Give the extent of all Plasmodium falciparum-infected red blood cells.
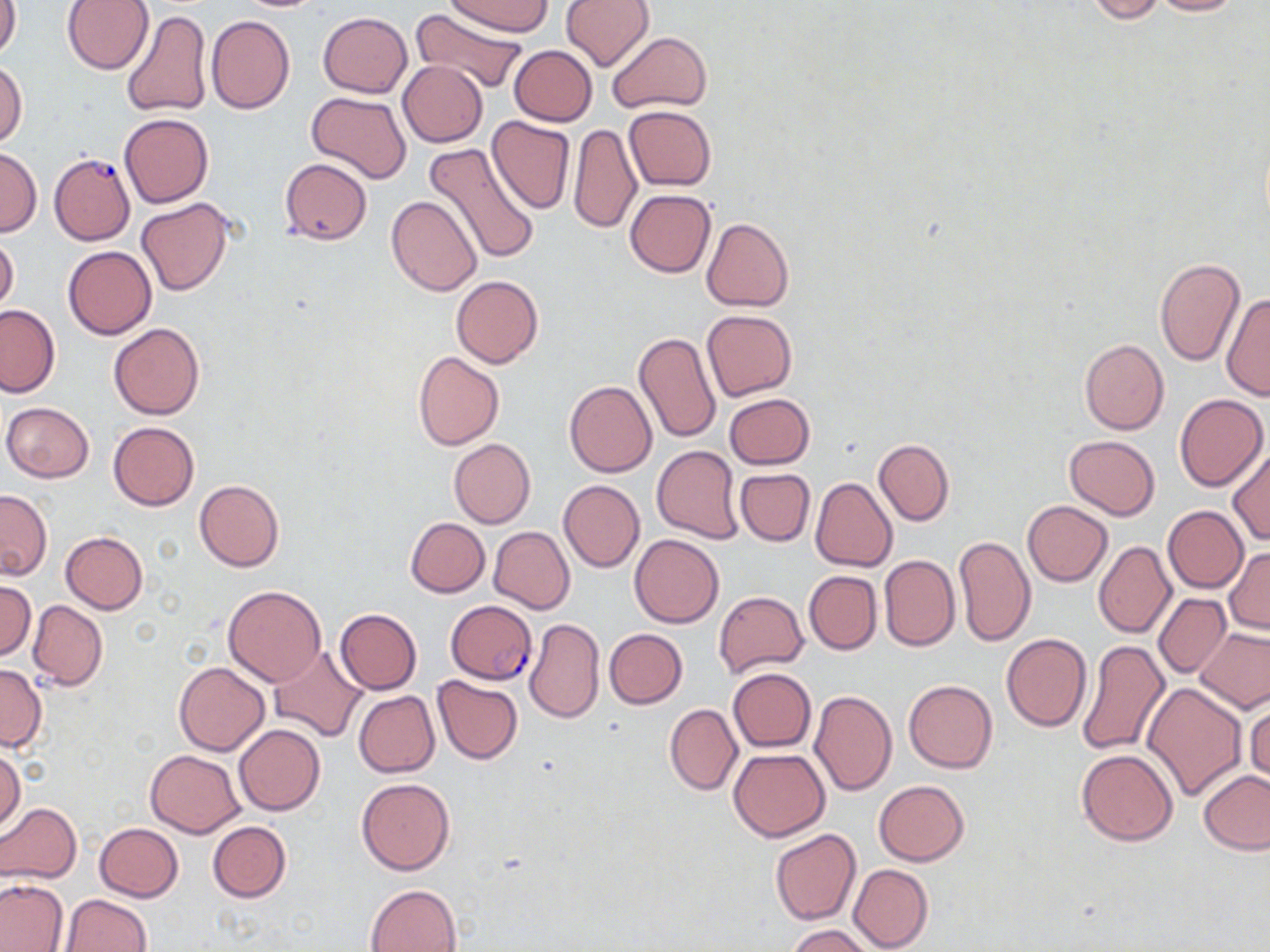

Approximate bounding boxes as (x1,y1)-(x2,y2) corner pairs in pixels.
Plasmodium falciparum-infected red blood cells: (51,154)-(135,248), (447,602)-(539,685).

Uninfected red blood cell locations: (61,0)-(153,74), (562,0)-(654,71), (1084,0)-(1167,23), (1148,0)-(1246,16), (0,1)-(21,62), (448,1)-(550,36), (411,6)-(527,96), (119,8)-(213,117), (318,12)-(413,97), (207,15)-(295,115), (608,31)-(712,114), (509,45)-(597,127), (397,60)-(488,147), (1,61)-(28,148), (306,92)-(412,184), (624,105)-(716,191), (119,113)-(213,208), (486,115)-(575,214), (568,124)-(642,234), (427,142)-(539,262), (0,147)-(42,237), (279,157)-(373,246), (625,189)-(716,278), (387,194)-(483,296), (137,198)-(234,296), (702,217)-(795,312), (0,235)-(19,313), (62,245)-(157,339), (1154,258)-(1243,366), (451,275)-(543,368), (1221,290)-(1270,400), (0,305)-(60,397), (701,309)-(798,402), (109,323)-(204,419), (633,332)-(721,444), (1080,338)-(1168,435), (413,352)-(504,450), (564,381)-(656,477), (723,393)-(814,470), (1174,395)-(1269,491), (3,402)-(94,482), (108,421)-(199,510), (1065,435)-(1159,520), (448,438)-(536,528), (873,438)-(954,525), (652,445)-(743,543), (1228,447)-(1270,546), (735,468)-(815,545), (811,477)-(897,572), (194,479)-(284,571), (559,480)-(645,572), (0,489)-(52,580), (1022,500)-(1112,586), (1163,506)-(1248,593), (406,517)-(490,597), (488,526)-(575,613), (60,532)-(148,613), (629,533)-(724,628), (953,537)-(1036,648), (1094,542)-(1176,639), (1225,547)-(1269,635), (879,555)-(960,653), (803,570)-(881,654), (0,581)-(36,661), (223,585)-(327,686), (714,590)-(808,678), (1154,594)-(1229,677), (28,600)-(108,690), (335,608)-(422,694), (525,618)-(605,723), (604,628)-(687,708), (1195,628)-(1270,714), (1002,633)-(1092,731), (1078,640)-(1171,756), (270,645)-(369,742), (174,661)-(269,756), (0,664)-(47,751), (727,668)-(817,752), (432,676)-(523,764), (903,680)-(997,773), (1142,681)-(1247,801), (354,690)-(440,777), (809,690)-(897,795), (1245,695)-(1270,789), (665,704)-(742,795), (233,723)-(326,815), (1,748)-(25,833), (728,748)-(830,840), (1076,748)-(1180,846), (145,749)-(244,837), (1199,772)-(1270,854), (357,777)-(455,876), (873,780)-(970,865), (0,803)-(82,884), (208,821)-(291,903), (94,823)-(183,902), (770,829)-(862,926), (847,864)-(933,951), (0,879)-(67,951), (366,883)-(462,952), (60,894)-(151,952), (786,925)-(873,952). Slide-level diagnosis: Plasmodium falciparum. Light microscopy. Thin blood film. Image is 1270×952 pixels. Single field of view. Captured at 1000x magnification. May-Grünwald-Giemsa-stained preparation.